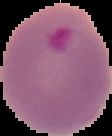

Summary:
  - Result: Plasmodium parasites detected
  - Image size: 112×136 pixels
  - Preparation: thin blood film
  - Image type: segmented cell region on a black background